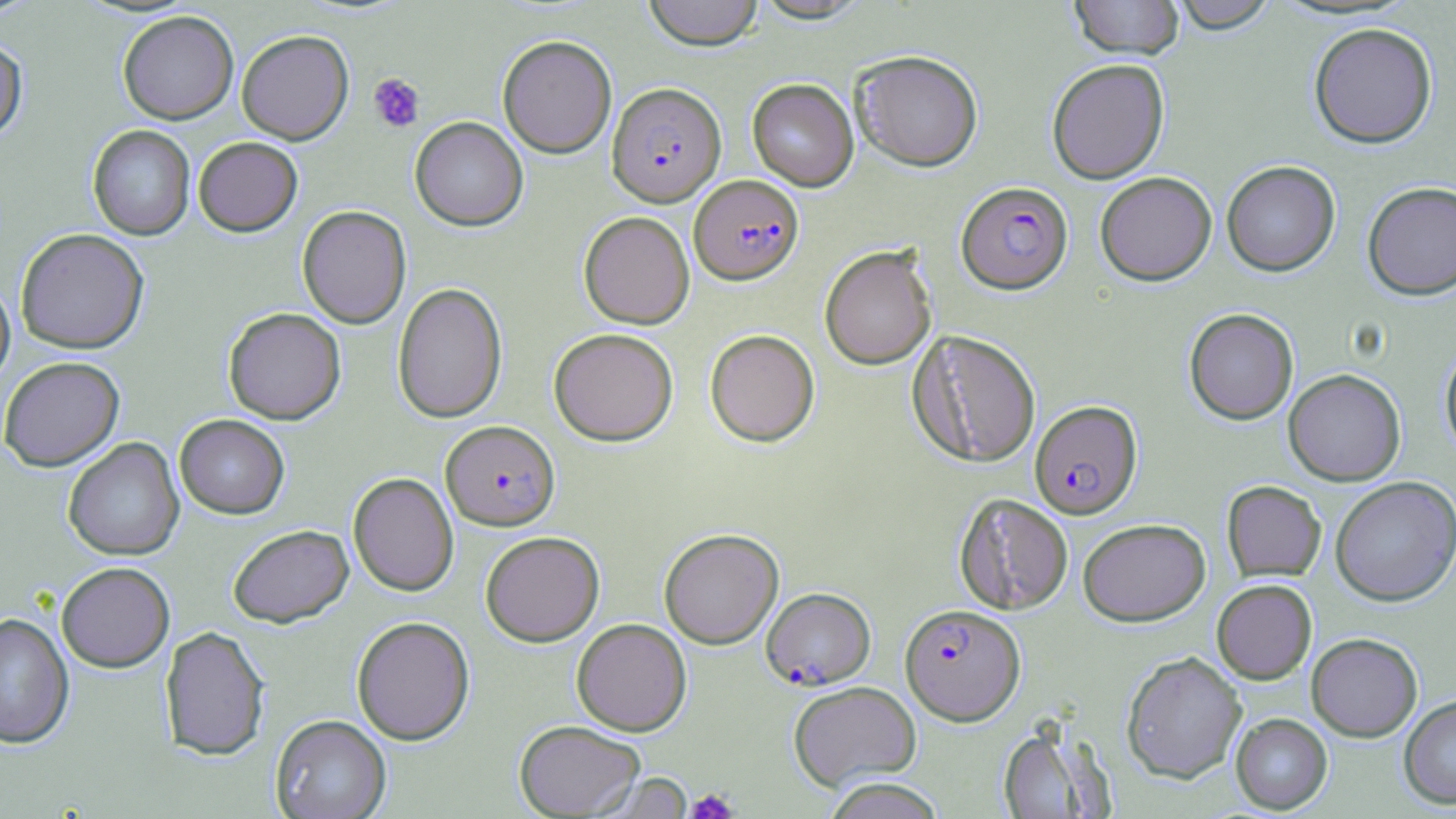 Approximate bounding boxes as (x1,y1)-(x2,y2) corner pairs in pixels. Plasmodium falciparum-infected red blood cell locations: (607,82)-(726,206), (689,175)-(804,285), (956,181)-(1072,294), (1030,399)-(1142,518), (441,420)-(560,530), (761,587)-(876,690), (900,603)-(1025,724). Platelet locations: (368,73)-(425,132), (686,788)-(738,819). Uninfected red blood cell locations: (643,0)-(763,51), (1069,0)-(1184,60), (1167,0)-(1280,33), (117,10)-(238,124), (1308,21)-(1438,149), (236,29)-(354,144), (498,34)-(617,158), (0,39)-(28,142), (850,49)-(984,172), (1046,58)-(1169,184), (747,78)-(859,191), (410,116)-(528,232), (87,124)-(195,240), (193,136)-(303,237), (1222,160)-(1340,276), (1095,171)-(1217,285), (1362,180)-(1456,300), (297,205)-(411,329), (578,211)-(694,329), (15,228)-(149,353), (819,244)-(937,370), (0,277)-(15,390), (392,282)-(507,423), (223,307)-(346,424), (1184,308)-(1298,424), (549,327)-(678,446), (705,329)-(820,447), (909,330)-(1042,468), (1439,343)-(1456,463), (0,356)-(124,472), (1283,369)-(1406,486), (174,414)-(289,519), (63,438)-(185,561), (349,472)-(459,596), (1330,476)-(1456,606), (1221,480)-(1326,582), (953,493)-(1074,615), (1078,518)-(1210,625), (228,524)-(354,627), (659,528)-(783,649), (480,530)-(605,646), (56,561)-(175,672), (1212,579)-(1317,684), (0,612)-(74,748), (351,616)-(475,745), (571,618)-(692,736), (160,626)-(270,761), (1306,632)-(1423,741), (1120,650)-(1247,784), (788,680)-(921,790), (1399,694)-(1456,809), (1230,713)-(1332,814), (271,714)-(391,819), (514,720)-(645,818), (997,723)-(1113,818), (594,772)-(695,818), (821,776)-(946,819). Slide-level diagnosis: Plasmodium falciparum. 1000x magnification. Thin blood smear. Image is 1456×819 pixels. Single field of view. May-Grünwald-Giemsa-stained preparation. Light microscopy.